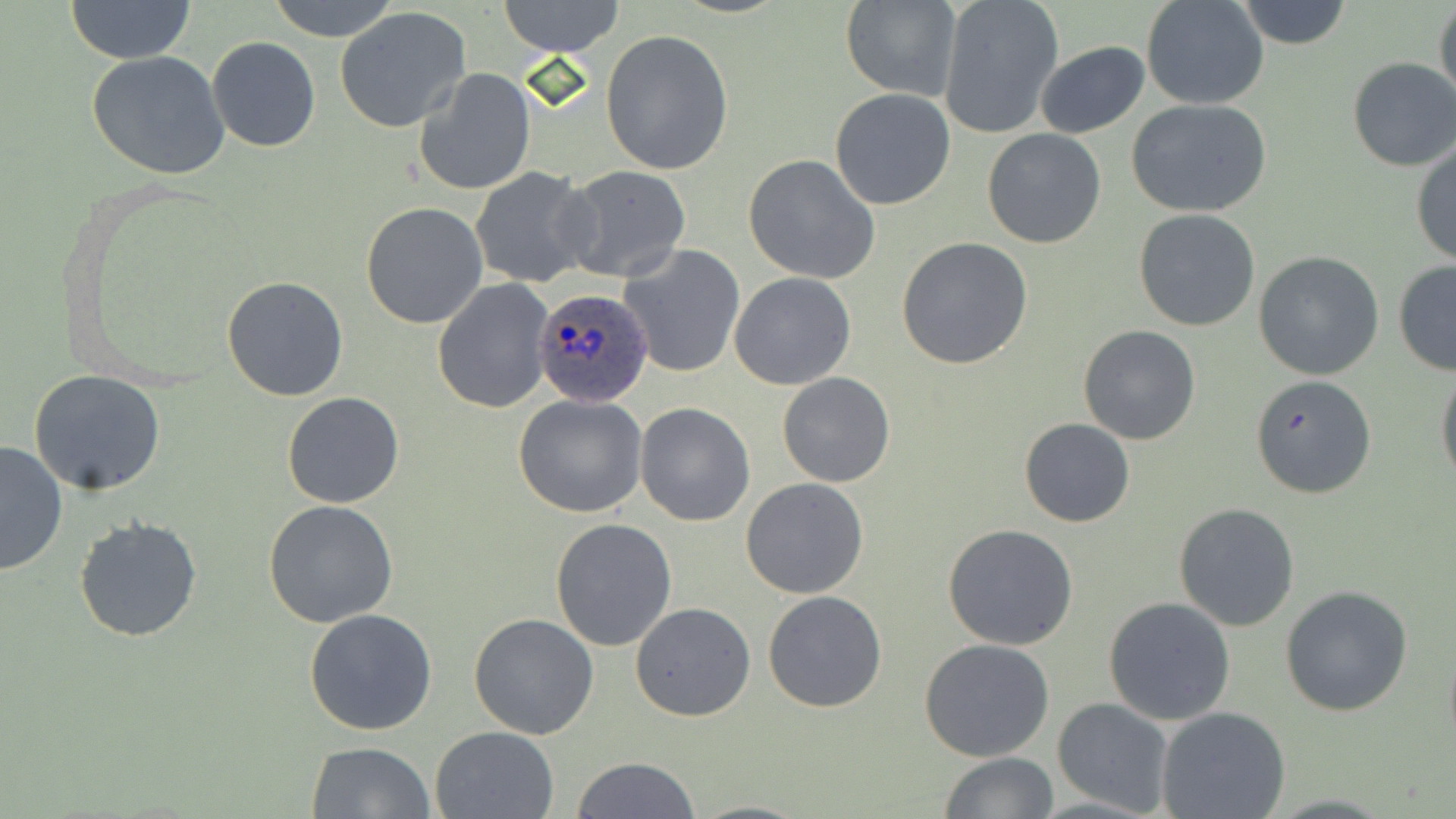
Summary:
  - Coordinate format: approximate bounding boxes as (x1,y1)-(x2,y2) corner pairs in pixels
  - Plasmodium ovale-infected red blood cell locations: (531,289)-(653,408)
  - Uninfected red blood cell locations: (64,0)-(198,64), (264,0)-(405,43), (498,0)-(625,56), (937,0)-(1062,138), (1142,0)-(1270,110), (1232,0)-(1353,49), (1432,0)-(1455,112), (840,1)-(961,102), (334,7)-(474,134), (601,29)-(733,178), (206,37)-(321,152), (1034,40)-(1150,138), (86,51)-(230,179), (1346,58)-(1456,172), (414,68)-(536,196), (830,88)-(956,211), (1126,98)-(1275,219), (981,128)-(1107,249), (1411,140)-(1456,268), (742,154)-(880,284), (557,164)-(691,282), (469,166)-(596,287), (360,201)-(488,329), (1133,209)-(1261,332), (896,236)-(1033,370), (619,244)-(746,378), (1254,251)-(1385,379), (1392,260)-(1456,377), (729,271)-(856,389), (222,276)-(349,401), (434,277)-(556,413), (1077,325)-(1201,445), (1435,364)-(1456,490), (28,371)-(167,495), (777,372)-(894,489), (1249,372)-(1378,499), (282,391)-(407,509), (513,393)-(649,518), (635,403)-(756,526), (1019,418)-(1136,528), (0,440)-(68,577), (739,477)-(869,600), (263,500)-(400,628), (1172,502)-(1300,632), (74,516)-(203,642), (549,518)-(678,651), (943,523)-(1078,650), (1280,585)-(1413,717), (763,591)-(887,711), (1102,596)-(1237,725), (630,601)-(756,721), (303,608)-(438,736), (469,613)-(599,740), (919,638)-(1055,761), (1052,698)-(1175,816), (1157,708)-(1291,819), (430,726)-(558,818), (305,741)-(437,819), (939,752)-(1058,819), (572,756)-(699,819)
  - Slide-level diagnosis: Plasmodium ovale
  - Modality: light microscopy
  - Image size: 1456×819 pixels
  - Preparation: thin blood film
  - Field of view: one of a larger specimen
  - Stain: May-Grünwald-Giemsa
  - Magnification: 1000x